Point out each malaria parasite.
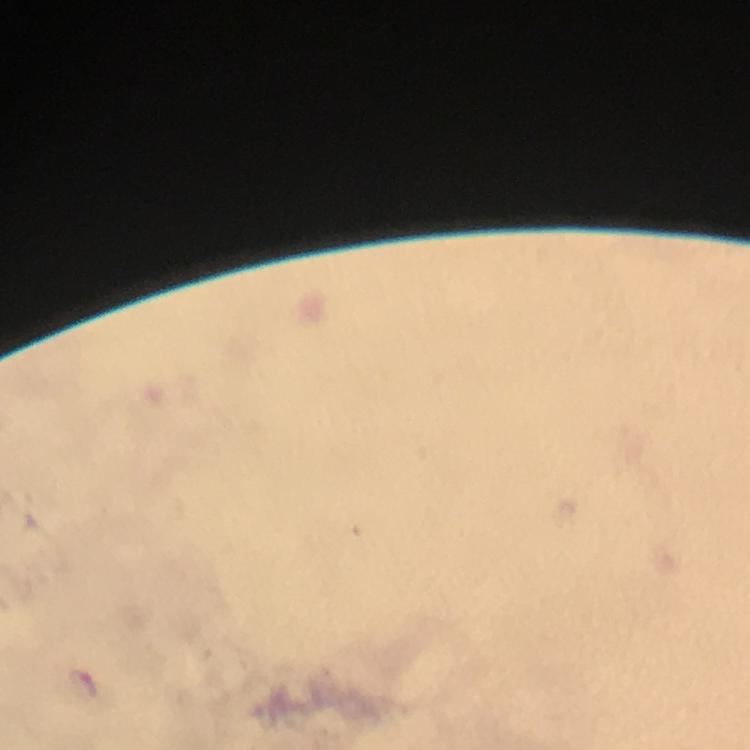
Approximate centers as {x, y} in pixels.
Malaria parasites: {82, 685}.

preparation = thick blood film
cropped from = a single field of view
stain = Giemsa
immersion oil = applied
capture = smartphone mounted on the microscope
context = from a malaria diagnostic workup
magnification = 100x
image size = 750×750 pixels